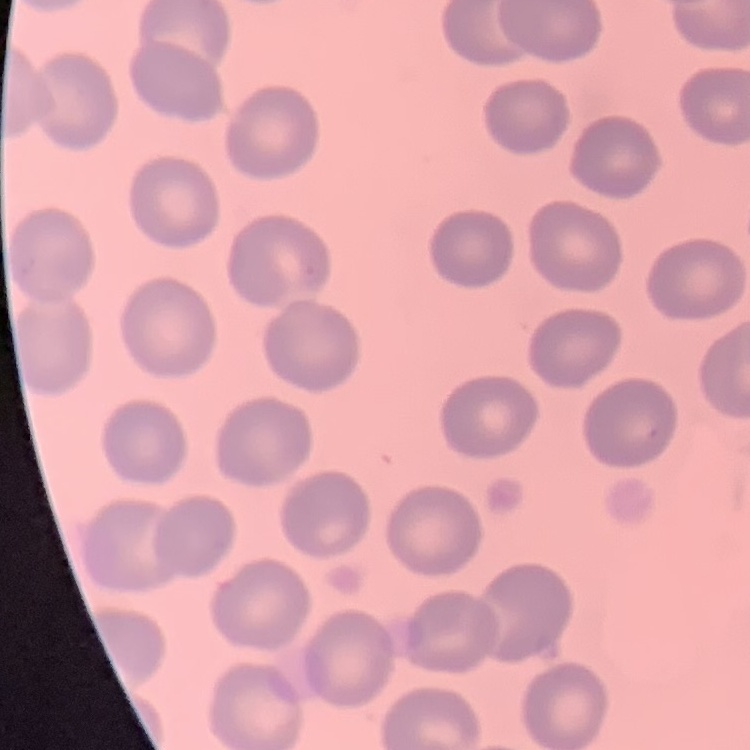
Summary:
  - Red blood cell morphology: no rouleaux formation
  - Stain: Field's or Giemsa
  - Preparation: thin blood smear
  - Image type: one tile cut from a larger photomicrograph